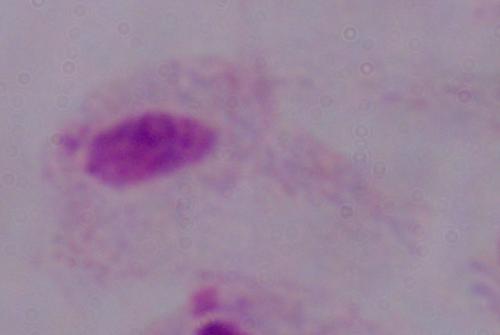
modality = micrograph
identification = trichomonad
magnification = 1000x